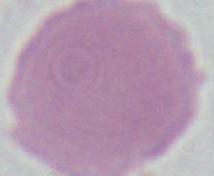
magnification = 1000x
modality = photomicrograph
identification = erythrocyte